Report the malaria status of this cell.
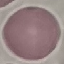

It is uninfected.

capture = smartphone camera at the microscope eyepiece
stain = Giemsa
preparation = thin blood smear
image type = automatically extracted cell patch, resized to 64 × 64 pixels